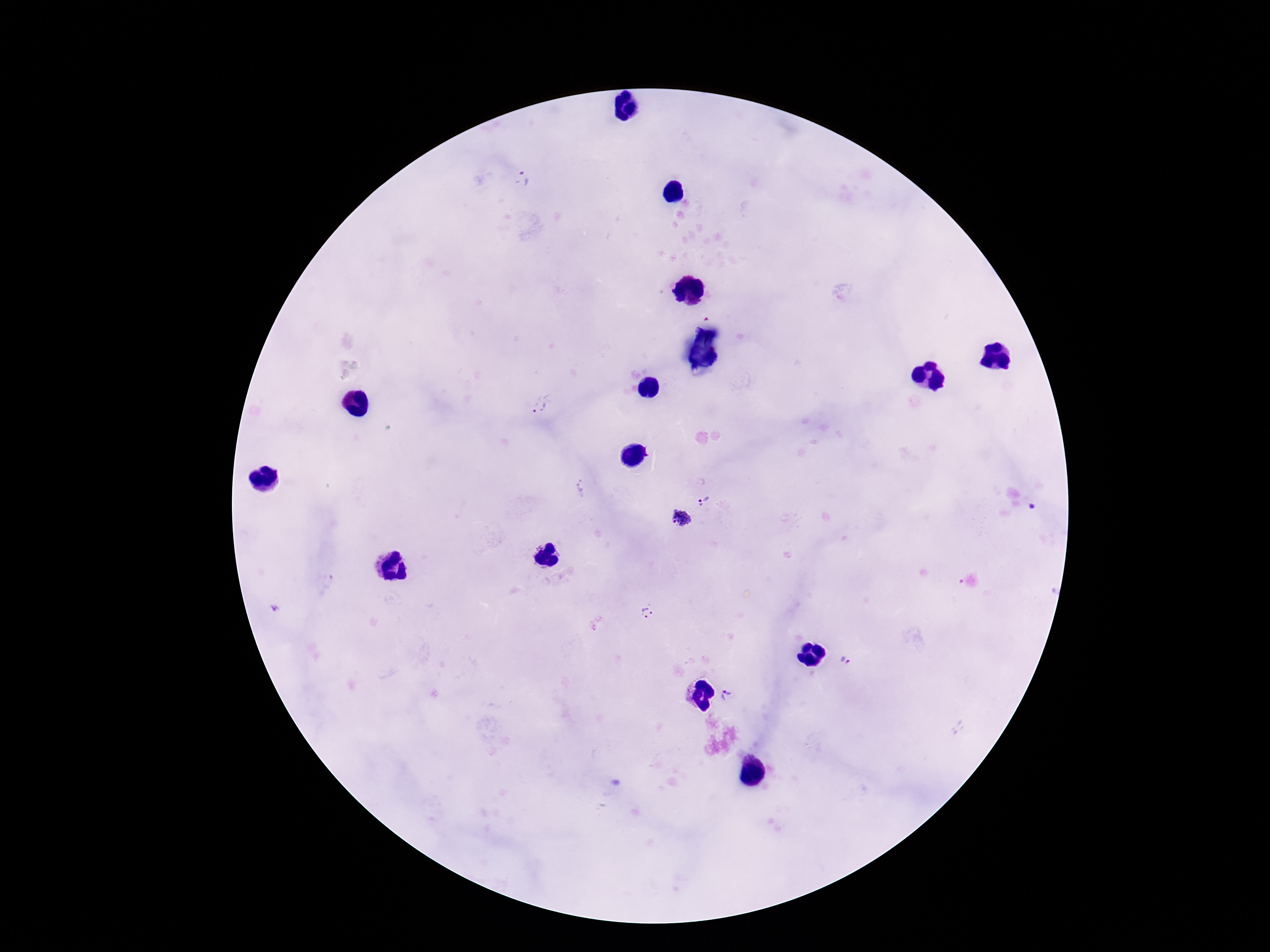
Plasmodium parasite locations = approximate object centers, in pixels from the top-left corner: (x=522, y=180), (x=540, y=405), (x=581, y=487), (x=704, y=500), (x=680, y=519), (x=647, y=612), (x=846, y=661), (x=728, y=695)
patient malaria status = positive
capture = smartphone camera through the microscope eyepiece
magnification = 100x
preparation = thick peripheral-blood smear
stain = Giemsa
image size = 1270×952 pixels
field of view = single